Assess the morphology of the erythrocytes.
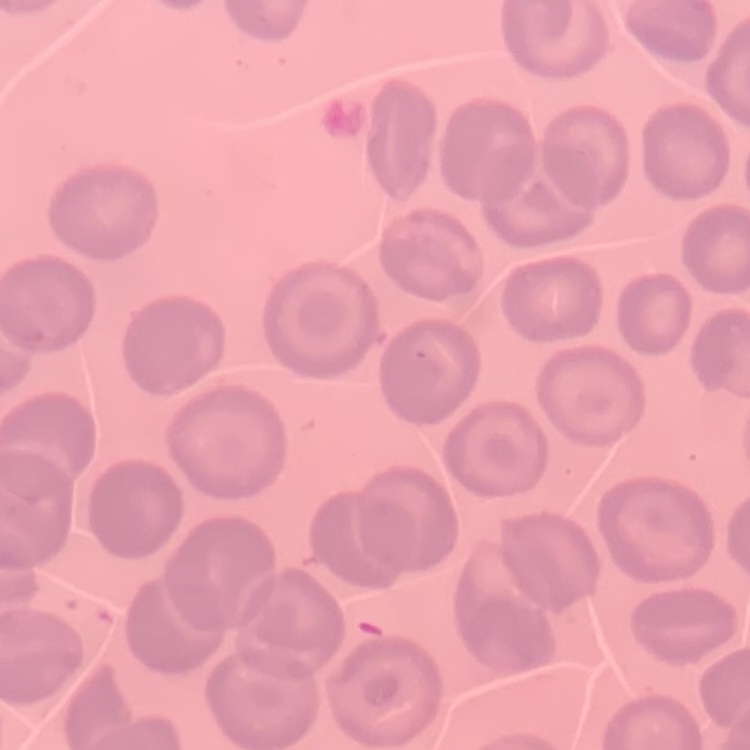

They show no rouleaux formation.

Thin peripheral smear. Stained with either Field's or Giemsa. Square crop of a larger photomicrograph.